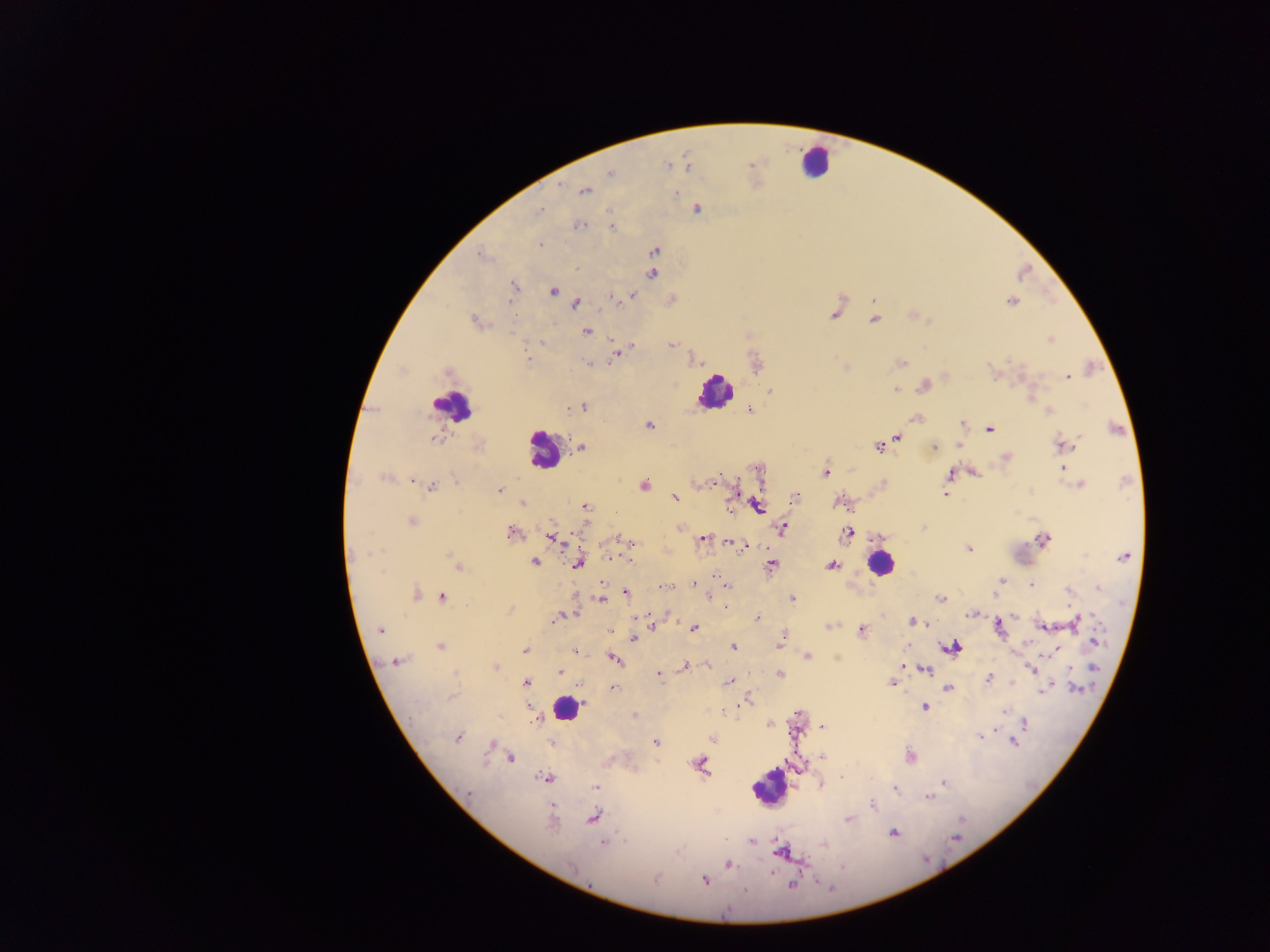
Approximate centers as (x, y) in pixels. Leukocyte locations: (814, 161), (714, 392), (451, 406), (542, 449), (880, 563), (565, 709), (768, 787). Plasmodium parasite locations: (668, 165), (750, 165), (610, 174), (585, 190), (676, 193), (697, 209), (539, 211), (579, 225), (611, 228), (539, 244), (654, 251), (479, 255), (576, 268), (652, 274), (514, 286), (553, 291), (633, 295), (613, 297), (872, 299), (510, 300), (1011, 301), (576, 303), (601, 311), (834, 316), (874, 320), (474, 321), (585, 331), (612, 338), (1050, 340), (542, 342), (671, 345), (630, 346), (617, 354), (528, 358), (900, 363), (590, 364), (991, 369), (447, 372), (1067, 377), (924, 386), (895, 389), (770, 390), (583, 406), (571, 408), (750, 410), (1048, 411), (916, 419), (648, 425), (963, 425), (989, 428), (433, 438), (898, 438), (879, 446), (959, 446), (1063, 446), (934, 447), (581, 448), (1005, 457), (1064, 470), (826, 472), (950, 475), (384, 477), (719, 478), (413, 479), (455, 481), (644, 485), (1081, 485), (431, 486), (947, 488), (500, 490), (946, 494), (673, 497), (795, 498), (839, 502), (522, 503), (758, 506), (586, 507), (412, 521), (679, 527), (783, 529), (511, 533), (848, 534), (550, 537), (617, 539), (703, 539), (1043, 539), (625, 540), (731, 542), (632, 543), (737, 545), (745, 546), (968, 549), (364, 553), (1125, 556), (450, 557), (610, 557), (631, 561), (534, 562), (577, 564), (771, 565), (831, 565), (458, 567), (1001, 580), (693, 584), (1031, 584), (727, 585), (663, 587), (1099, 588), (1068, 589), (625, 592), (416, 593), (995, 594), (443, 597), (710, 598), (600, 599), (940, 599), (791, 600), (510, 610), (970, 614), (558, 618), (757, 618), (913, 621), (1076, 621), (652, 625), (829, 626), (1044, 627), (694, 628), (999, 628), (380, 630), (609, 631), (862, 631), (782, 636), (633, 639), (780, 641), (1096, 641), (440, 647), (952, 647), (733, 648), (525, 650), (575, 650), (808, 656), (614, 659), (397, 660), (684, 666), (901, 666), (496, 667), (1032, 668), (1094, 669), (925, 670), (559, 672), (659, 675), (780, 675), (989, 678), (730, 681), (526, 682), (891, 683), (580, 685), (613, 688), (948, 689), (1046, 689), (1076, 689), (451, 696), (746, 701), (925, 706), (1005, 712), (797, 713), (634, 715), (1025, 722), (770, 725), (823, 727), (981, 735), (458, 738), (712, 738), (1013, 742), (552, 743), (656, 743), (491, 745), (822, 757), (909, 757), (510, 759), (700, 765), (544, 779), (943, 783), (821, 784), (597, 786), (895, 789), (469, 793), (929, 797), (872, 805), (593, 817), (848, 820), (551, 823), (893, 834), (751, 842), (603, 843), (781, 851), (729, 865), (572, 866), (655, 879), (705, 881), (792, 885). Single field of view. Collected in Ghana. Image is 1270×952 pixels. Photographed through a microscope with a mobile-phone camera. Thick blood smear.